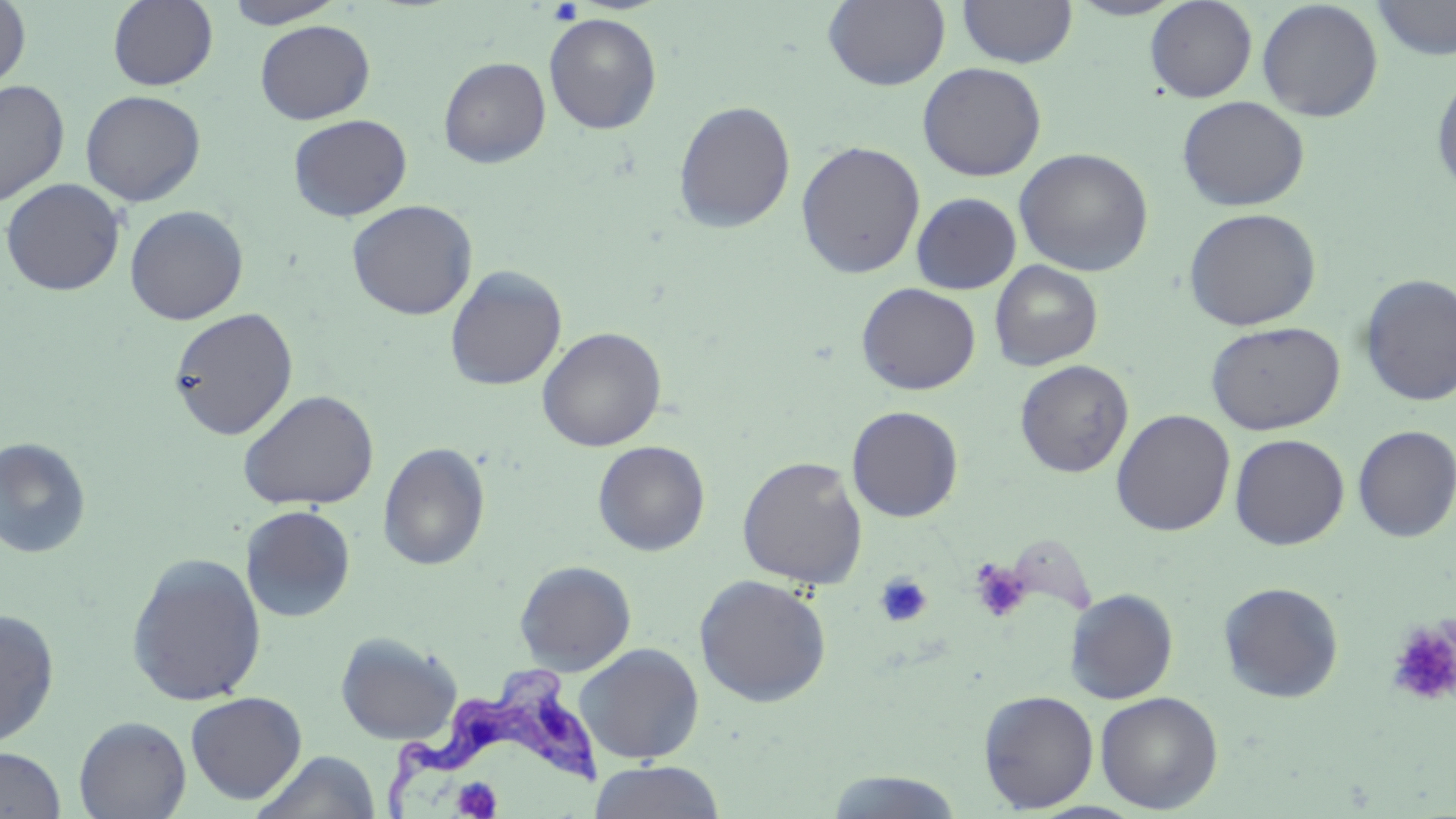
Summary:
  - Coordinate format: approximate bounding boxes as [x1, y1, x2, y2] in pixels
  - Platelet locations: [547, 1, 583, 26], [969, 559, 1033, 624], [875, 572, 932, 628], [1386, 622, 1456, 707], [449, 778, 505, 817]
  - Uninfected red blood cell locations: [0, 0, 31, 93], [107, 0, 218, 91], [223, 0, 347, 29], [823, 0, 950, 91], [956, 0, 1077, 68], [1066, 0, 1189, 20], [1144, 0, 1258, 103], [1371, 0, 1456, 60], [1256, 1, 1384, 122], [544, 12, 662, 134], [254, 19, 375, 124], [439, 56, 551, 168], [917, 62, 1047, 181], [1431, 71, 1456, 197], [0, 79, 70, 207], [80, 90, 205, 207], [1176, 96, 1309, 212], [672, 100, 796, 234], [288, 114, 412, 221], [795, 140, 925, 279], [1015, 148, 1154, 277], [0, 178, 126, 296], [911, 192, 1022, 294], [346, 199, 478, 320], [124, 205, 248, 325], [1184, 207, 1321, 331], [989, 260, 1103, 371], [444, 265, 567, 390], [1358, 274, 1455, 406], [856, 282, 981, 395], [168, 307, 298, 440], [1205, 321, 1346, 435], [536, 326, 667, 452], [1014, 359, 1133, 478], [237, 389, 379, 511], [846, 406, 963, 522], [1111, 409, 1235, 536], [1352, 425, 1456, 543], [1229, 434, 1349, 550], [0, 437, 92, 559], [592, 440, 710, 556], [377, 442, 490, 570], [736, 456, 868, 589], [240, 505, 356, 623], [125, 552, 267, 707], [514, 560, 636, 674], [694, 573, 832, 707], [1218, 581, 1344, 703], [1064, 588, 1179, 704], [0, 608, 60, 748], [335, 632, 462, 745], [573, 642, 705, 764], [978, 690, 1099, 812], [185, 691, 307, 804], [1094, 691, 1223, 813], [74, 715, 192, 818], [0, 746, 66, 819], [253, 750, 381, 819], [588, 760, 727, 819], [822, 771, 966, 818]
  - Trypanosoma brucei locations: [385, 667, 618, 815]
  - Slide-level diagnosis: Trypanosoma brucei
  - Image size: 1456×819 pixels
  - Magnification: 1000x
  - Modality: optical microscopy
  - Field of view: one of a larger specimen
  - Stain: May-Grünwald-Giemsa
  - Preparation: thin blood film